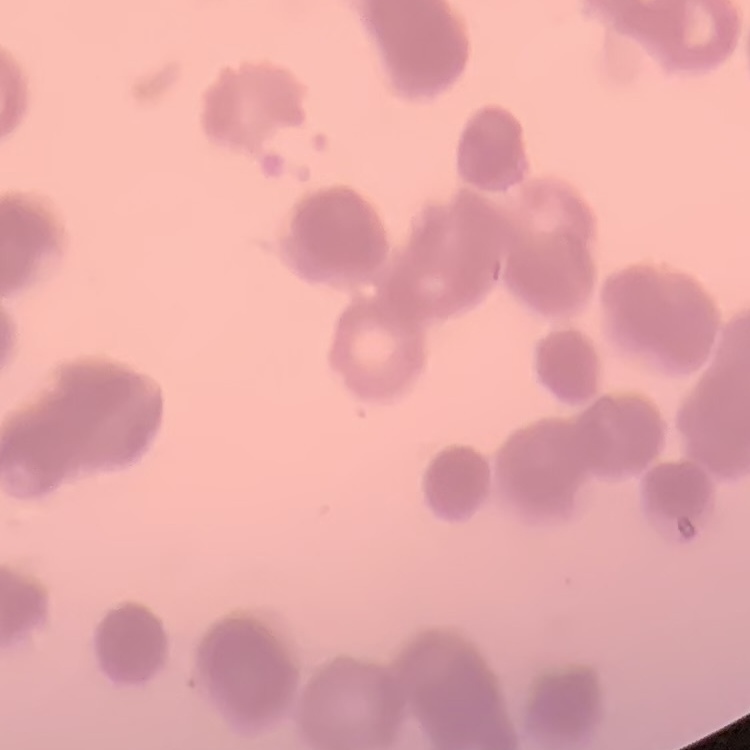

erythrocyte morphology = rouleaux formation
stain = Field's or Giemsa
preparation = thin blood smear
image type = one tile cut from a larger photomicrograph